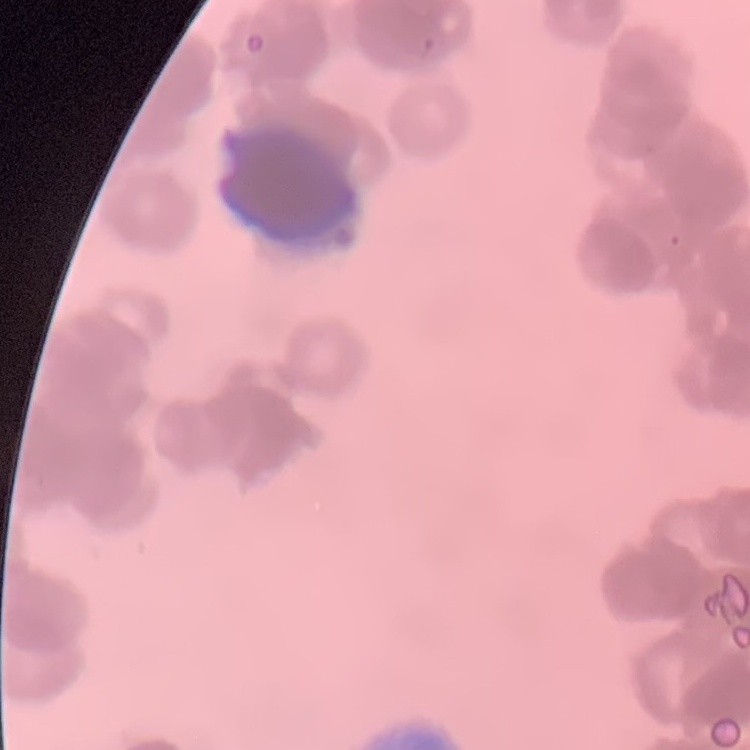

erythrocyte morphology = rouleaux formation
preparation = thin blood film
stain = Field's or Giemsa
image type = one tile cut from a larger photomicrograph